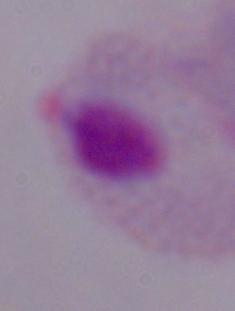

Micrograph. A trichomonad is seen. 1000x magnification.